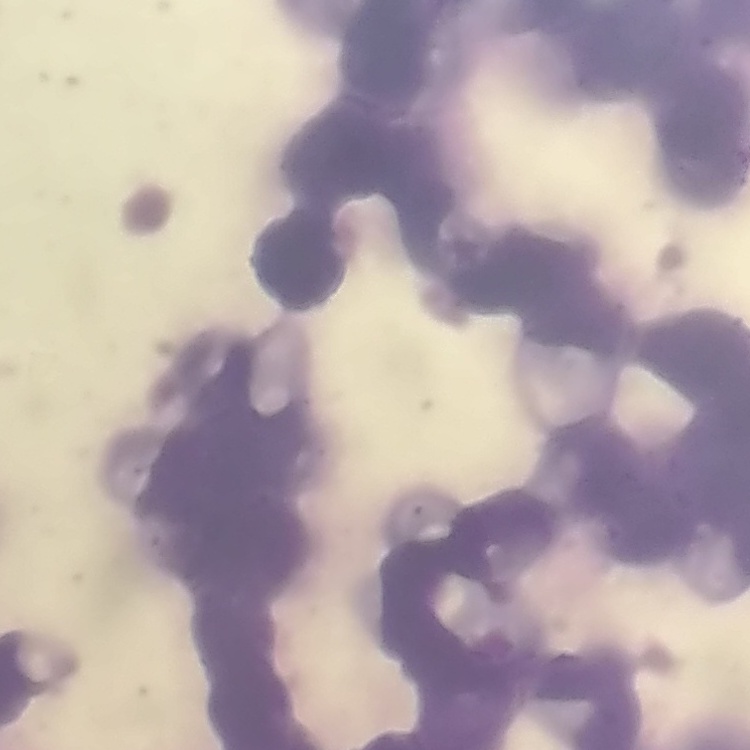
The erythrocytes exhibit rouleaux formation. Stained with either Field's or Giemsa. Thin peripheral smear. Square crop of a larger photomicrograph.